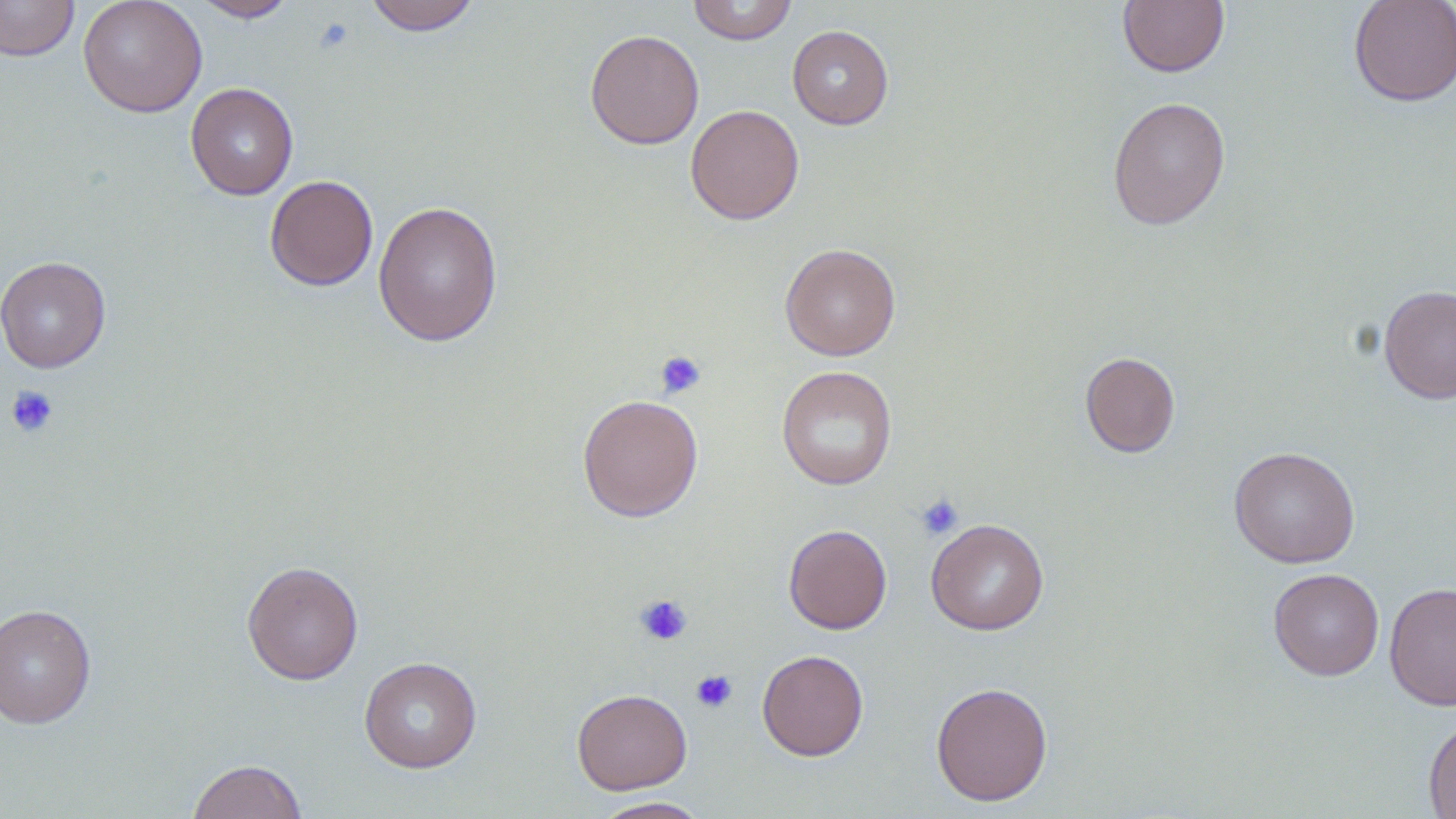
Approximate bounding boxes as (x1, y1, x2, y2) in pixels. Uninfected red blood cell locations: (0, 0, 79, 61), (78, 0, 208, 118), (190, 0, 298, 22), (363, 0, 482, 35), (687, 0, 798, 45), (1117, 0, 1229, 77), (1348, 0, 1456, 107), (787, 25, 893, 129), (585, 29, 705, 150), (185, 82, 298, 200), (1107, 96, 1231, 230), (685, 104, 805, 224), (264, 174, 378, 291), (373, 200, 503, 347), (780, 243, 901, 361), (0, 255, 111, 373), (1378, 283, 1456, 404), (1079, 351, 1180, 457), (776, 365, 897, 490), (577, 393, 703, 522), (1229, 446, 1360, 568), (926, 518, 1049, 634), (783, 524, 892, 634), (242, 560, 364, 685), (1268, 568, 1384, 680), (1384, 581, 1456, 710), (0, 603, 96, 728), (757, 649, 869, 761), (359, 656, 482, 773), (930, 681, 1053, 806), (571, 688, 692, 795), (1423, 717, 1456, 818), (187, 758, 307, 819), (591, 796, 713, 818). Platelet locations: (313, 17, 354, 54), (654, 350, 707, 400), (5, 384, 59, 439), (915, 493, 964, 541), (634, 593, 693, 646), (691, 669, 737, 712). Slide-level diagnosis: negative for blood parasites. Light microscopy. Captured at 1000x magnification. Thin blood film. May-Grünwald-Giemsa stain. Image is 1456×819 pixels. One field of a larger specimen.